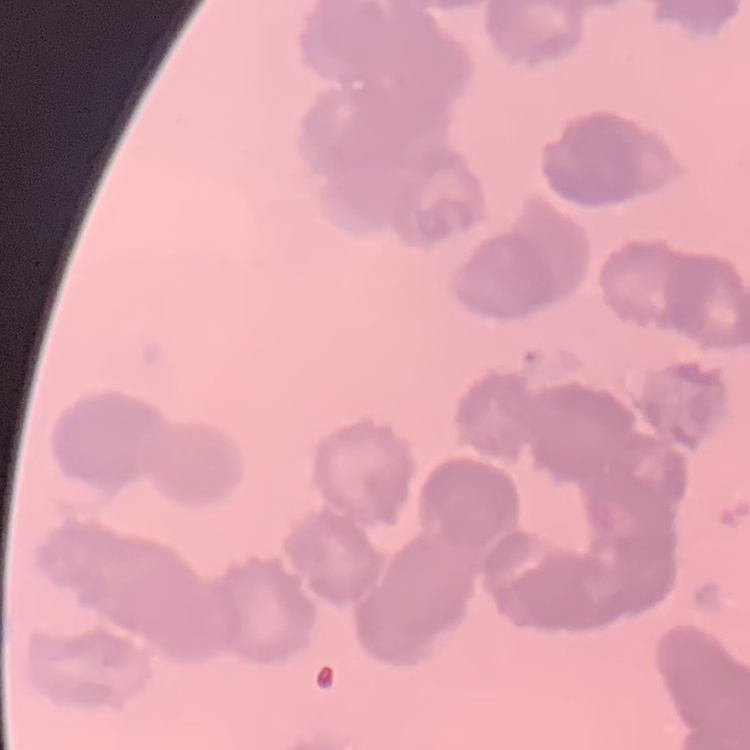

The erythrocytes show rouleaux formation. Thin peripheral smear. Field's or Giemsa stain. Square crop of a larger photomicrograph.